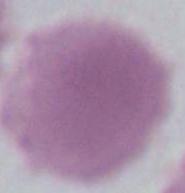

Summary:
  - Magnification: 1000x
  - Modality: photomicrograph
  - Identification: erythrocyte